Outline each P. falciparum parasite and classify it by life-cycle stage.
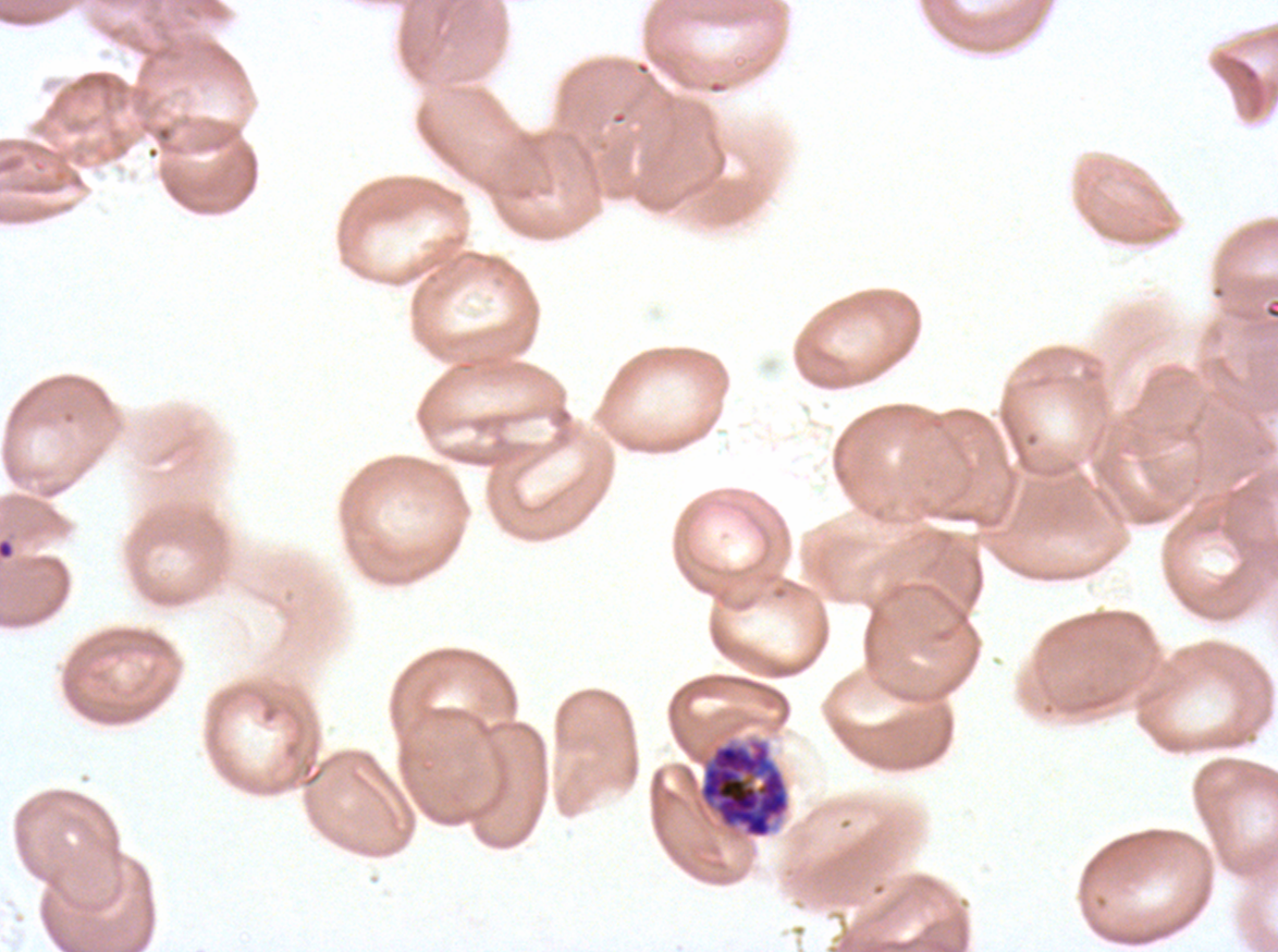
Approximate bounding boxes as (x1, y1, x2, y2) in pixels.
Early schizonts: (699, 739, 790, 838).
No rings, late-ring/early-trophozoite forms, mid trophozoites, late trophozoites, late schizonts, segmenters, or gametocytes observed.

stain = Giemsa
field of view = sub-image separated from a larger composite
image size = 1278×952 pixels
specimen = P. falciparum cultured ex vivo for 24 to 48 hours, from a patient in The Gambia
preparation = thin blood smear